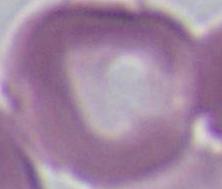

Summary:
  - Modality: photomicrograph
  - Identification: erythrocyte
  - Magnification: 1000x